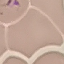
Result: negative for malaria parasites. Photographed with a smartphone camera at the microscope eyepiece. Cell patch, automatically extracted from a larger field of view and resized to 64 × 64 pixels. Thin blood smear. Giemsa-stained preparation.